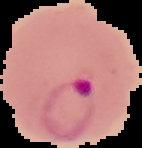
Summary:
  - Image size: 142×148 pixels
  - Image type: segmented cell region with the area outside set to black
  - Malaria status: parasitized
  - Preparation: thin blood film